Identify the blood parasite species.
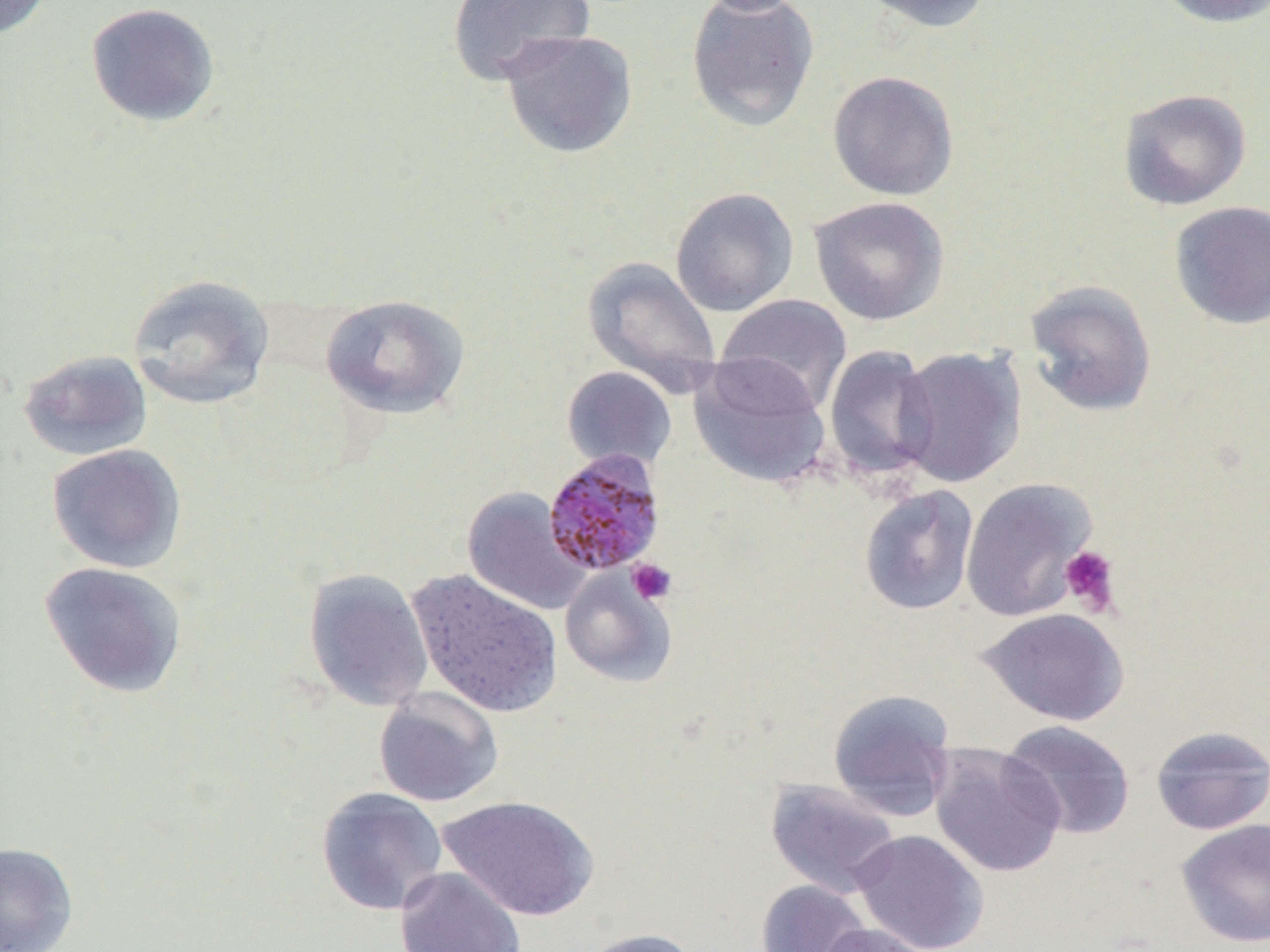
Plasmodium malariae.

magnification = 1000x
platelet locations = approximate bounding boxes as [x1, y1, x2, y2] in pixels: [1058, 545, 1122, 618], [627, 558, 677, 605]
uninfected red blood cell locations = approximate bounding boxes as [x1, y1, x2, y2] in pixels: [0, 0, 53, 40], [695, 0, 811, 16], [855, 0, 996, 33], [1152, 0, 1270, 28], [86, 1, 220, 128], [447, 1, 594, 85], [686, 1, 820, 132], [498, 29, 638, 158], [827, 70, 959, 201], [1118, 88, 1251, 211], [669, 187, 799, 316], [809, 195, 950, 325], [1168, 200, 1270, 330], [582, 256, 723, 393], [128, 274, 276, 410], [1023, 279, 1158, 418], [320, 294, 471, 419], [715, 294, 852, 413], [823, 345, 939, 483], [894, 345, 1027, 488], [17, 349, 153, 461], [688, 356, 831, 490], [561, 366, 677, 472], [46, 444, 187, 574], [960, 477, 1097, 622], [859, 485, 979, 615], [462, 487, 592, 615], [39, 562, 188, 698], [559, 566, 678, 688], [302, 567, 434, 712], [406, 568, 563, 718], [976, 608, 1130, 726], [373, 688, 504, 807], [828, 688, 957, 820], [1000, 720, 1135, 840], [1150, 725, 1270, 835], [928, 743, 1067, 879], [765, 779, 903, 898], [316, 787, 448, 916], [437, 795, 600, 921], [1176, 819, 1270, 948], [851, 829, 989, 952], [0, 841, 79, 952], [395, 866, 526, 952], [755, 880, 872, 952], [815, 923, 934, 952], [576, 927, 702, 952]
image size = 1270×952 pixels
field of view = one of a larger specimen
modality = light microscopy
preparation = thin blood film
Plasmodium malariae-infected red blood cell locations = approximate bounding boxes as [x1, y1, x2, y2] in pixels: [542, 450, 666, 577]